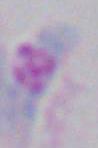
{
  "identification": "Toxoplasma gondii",
  "modality": "photomicrograph",
  "magnification": "1000x"
}